Report the malaria status of this cell.
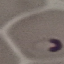

Parasitized.

Summary:
  - Image type: cell patch, automatically extracted from a larger field of view and resized to 64 × 64 pixels
  - Preparation: thin blood smear
  - Capture: smartphone through the microscope eyepiece
  - Stain: Giemsa